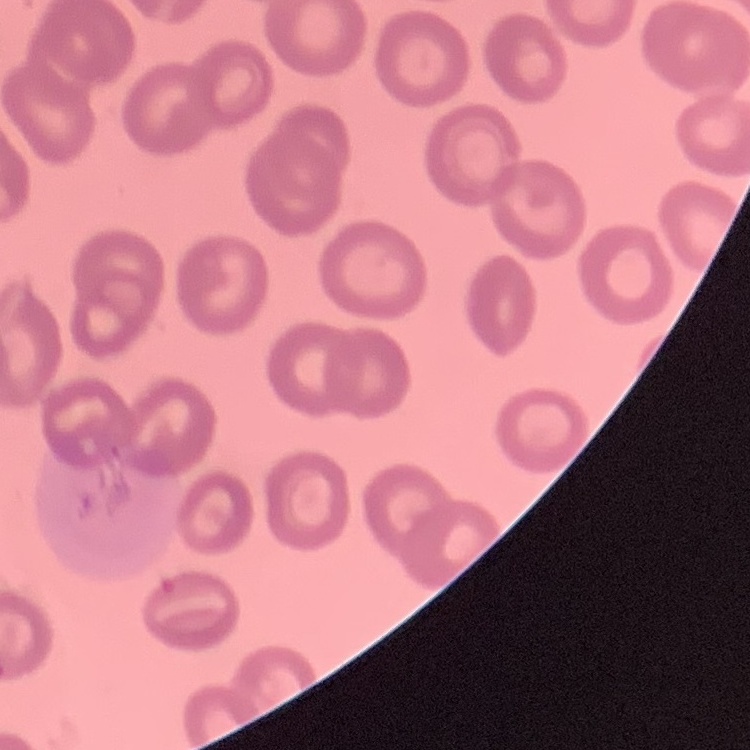
red_blood_cell_morphology: no rouleaux formation
stain: Field's or Giemsa
image_type: square crop of a larger photomicrograph
preparation: thin peripheral smear